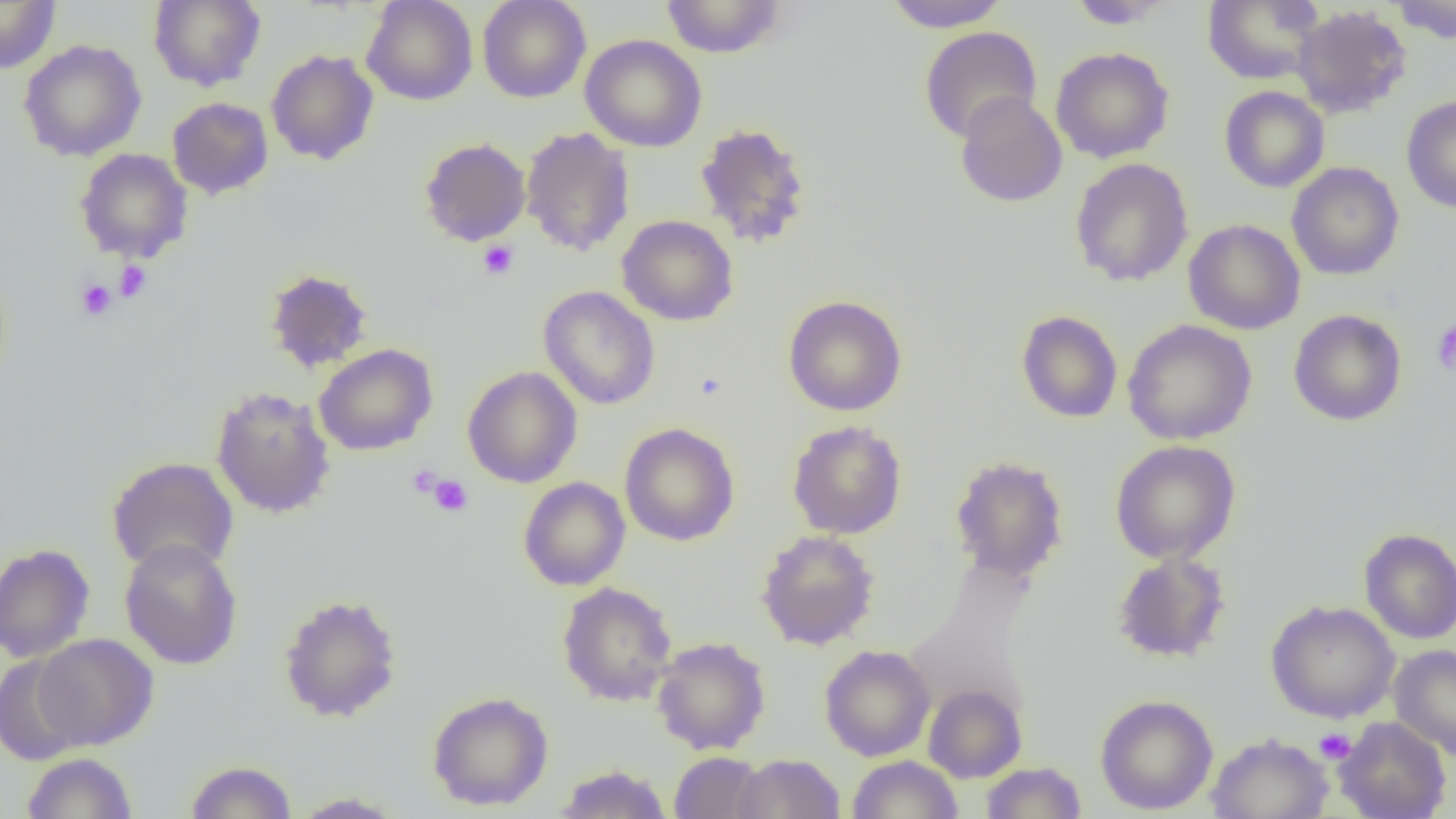
slide_level_diagnosis: negative for blood parasites
preparation: thin blood film
uninfected_red_blood_cell_locations: 'approximate bounding boxes as (x1, y1, x2, y2) in pixels: (148, 0, 266, 91), (362, 0, 478, 106), (477, 0, 591, 103), (660, 0, 787, 58), (879, 0, 1012, 31), (1202, 0, 1324, 86), (1389, 0, 1456, 43), (0, 1, 62, 74), (1065, 1, 1177, 29), (1291, 5, 1412, 119), (919, 26, 1042, 144), (580, 34, 707, 153), (18, 39, 146, 162), (1050, 47, 1174, 163), (266, 49, 379, 166), (1219, 86, 1330, 193), (954, 91, 1068, 208), (1401, 95, 1456, 213), (167, 97, 274, 200), (1249, 111, 1366, 250), (694, 123, 812, 248), (520, 126, 636, 257), (419, 137, 531, 247), (75, 148, 193, 264), (1069, 158, 1194, 287), (1287, 161, 1404, 280), (616, 214, 739, 326), (1183, 219, 1306, 335), (263, 268, 374, 374), (539, 285, 660, 410), (782, 294, 908, 416), (1015, 309, 1123, 424), (1288, 309, 1407, 426), (1014, 314, 1248, 425), (1123, 319, 1258, 445), (313, 343, 439, 456), (462, 366, 582, 488), (210, 386, 336, 518), (786, 420, 908, 539), (619, 422, 740, 547), (1110, 439, 1241, 564), (949, 455, 1069, 584), (106, 456, 239, 576), (518, 477, 631, 591), (1359, 528, 1456, 644), (756, 530, 879, 650), (119, 537, 243, 670), (0, 544, 95, 662), (1111, 551, 1232, 663), (557, 582, 678, 707), (278, 593, 403, 723), (1265, 599, 1400, 723), (32, 633, 159, 750), (651, 636, 771, 755), (1389, 644, 1456, 761), (819, 645, 935, 761), (0, 653, 87, 765), (923, 683, 1027, 782), (427, 690, 554, 811), (1095, 694, 1218, 815), (1334, 716, 1451, 819), (1205, 732, 1334, 819), (669, 751, 768, 819), (21, 752, 138, 818), (731, 753, 845, 818), (848, 755, 963, 819), (184, 760, 298, 818), (979, 761, 1087, 819), (552, 764, 674, 818), (289, 791, 406, 818)'
image_size: 1456×819 pixels
platelet_locations: 'approximate bounding boxes as (x1, y1, x2, y2) in pixels: (478, 240, 520, 280), (114, 260, 152, 302), (74, 278, 118, 322), (1431, 321, 1456, 376), (408, 464, 442, 497), (429, 475, 473, 517), (1315, 728, 1356, 763)'
magnification: 1000x
modality: optical microscopy
field_of_view: one of a larger specimen